Assess this cell for malaria.
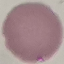
It is uninfected.

Summary:
  - Capture: smartphone through the microscope eyepiece
  - Stain: Giemsa
  - Preparation: thin smear
  - Image type: cell patch, automatically extracted from a larger field of view and resized to 64 × 64 pixels